Assess this cell for malaria.
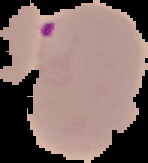

It is parasitized.

Summary:
  - Image size: 148×163 pixels
  - Image type: segmented cell region on a black background
  - Preparation: thin blood film